Identify the parasite.
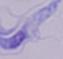

This is a trypanosome.

{
  "modality": "photomicrograph",
  "magnification": "1000x"
}